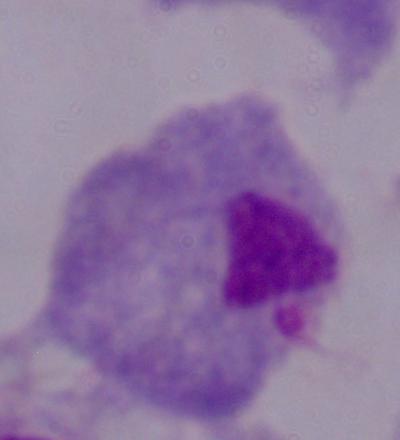

magnification = 1000x
identification = trichomonad
modality = photomicrograph